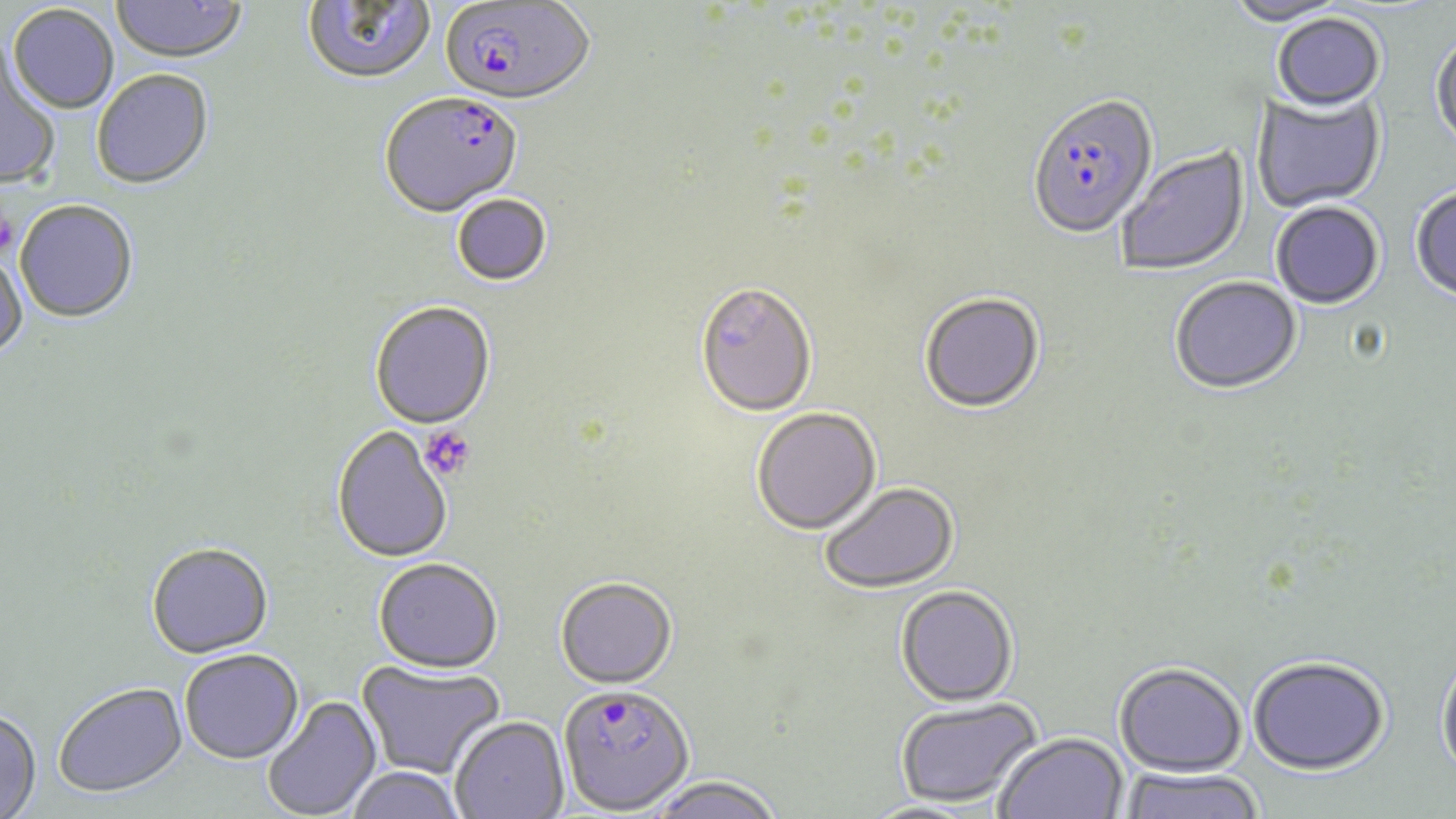
slide_level_diagnosis: Plasmodium falciparum
stain: May-Grünwald-Giemsa
image_size: 1456×819 pixels
field_of_view: single
magnification: 1000x
platelet_locations: 'approximate bounding boxes as named x1/y1/x2/y2 corners in pixels: (x1=0, y1=207, x2=17, y2=258), (x1=419, y1=425, x2=475, y2=481)'
uninfected_red_blood_cell_locations: 'approximate bounding boxes as named x1/y1/x2/y2 corners in pixels: (x1=302, y1=0, x2=437, y2=87), (x1=1224, y1=0, x2=1353, y2=28), (x1=112, y1=1, x2=247, y2=66), (x1=8, y1=6, x2=119, y2=116), (x1=1272, y1=14, x2=1386, y2=114), (x1=1430, y1=33, x2=1456, y2=155), (x1=0, y1=48, x2=60, y2=190), (x1=92, y1=71, x2=214, y2=191), (x1=1253, y1=90, x2=1387, y2=213), (x1=1116, y1=145, x2=1250, y2=277), (x1=1410, y1=187, x2=1456, y2=305), (x1=452, y1=194, x2=553, y2=288), (x1=14, y1=202, x2=138, y2=325), (x1=1271, y1=203, x2=1384, y2=311), (x1=0, y1=247, x2=27, y2=362), (x1=1170, y1=278, x2=1302, y2=398), (x1=695, y1=285, x2=817, y2=419), (x1=919, y1=294, x2=1045, y2=416), (x1=370, y1=303, x2=496, y2=431), (x1=751, y1=408, x2=882, y2=535), (x1=331, y1=427, x2=452, y2=565), (x1=819, y1=483, x2=960, y2=594), (x1=147, y1=545, x2=274, y2=660), (x1=373, y1=559, x2=502, y2=675), (x1=554, y1=577, x2=678, y2=690), (x1=895, y1=587, x2=1018, y2=708), (x1=180, y1=651, x2=304, y2=765), (x1=1436, y1=655, x2=1456, y2=785), (x1=1247, y1=659, x2=1389, y2=778), (x1=356, y1=660, x2=506, y2=779), (x1=1114, y1=664, x2=1246, y2=778), (x1=53, y1=682, x2=189, y2=800), (x1=262, y1=694, x2=384, y2=819), (x1=894, y1=698, x2=1041, y2=807), (x1=0, y1=709, x2=42, y2=818), (x1=450, y1=716, x2=569, y2=818), (x1=994, y1=733, x2=1127, y2=819), (x1=344, y1=767, x2=466, y2=819), (x1=1119, y1=769, x2=1265, y2=819), (x1=645, y1=776, x2=785, y2=819)'
preparation: thin blood film
modality: optical microscopy
plasmodium_falciparum_infected_red_blood_cell_locations: 'approximate bounding boxes as named x1/y1/x2/y2 corners in pixels: (x1=440, y1=1, x2=594, y2=108), (x1=380, y1=94, x2=523, y2=220), (x1=1026, y1=97, x2=1158, y2=242), (x1=558, y1=684, x2=694, y2=814)'